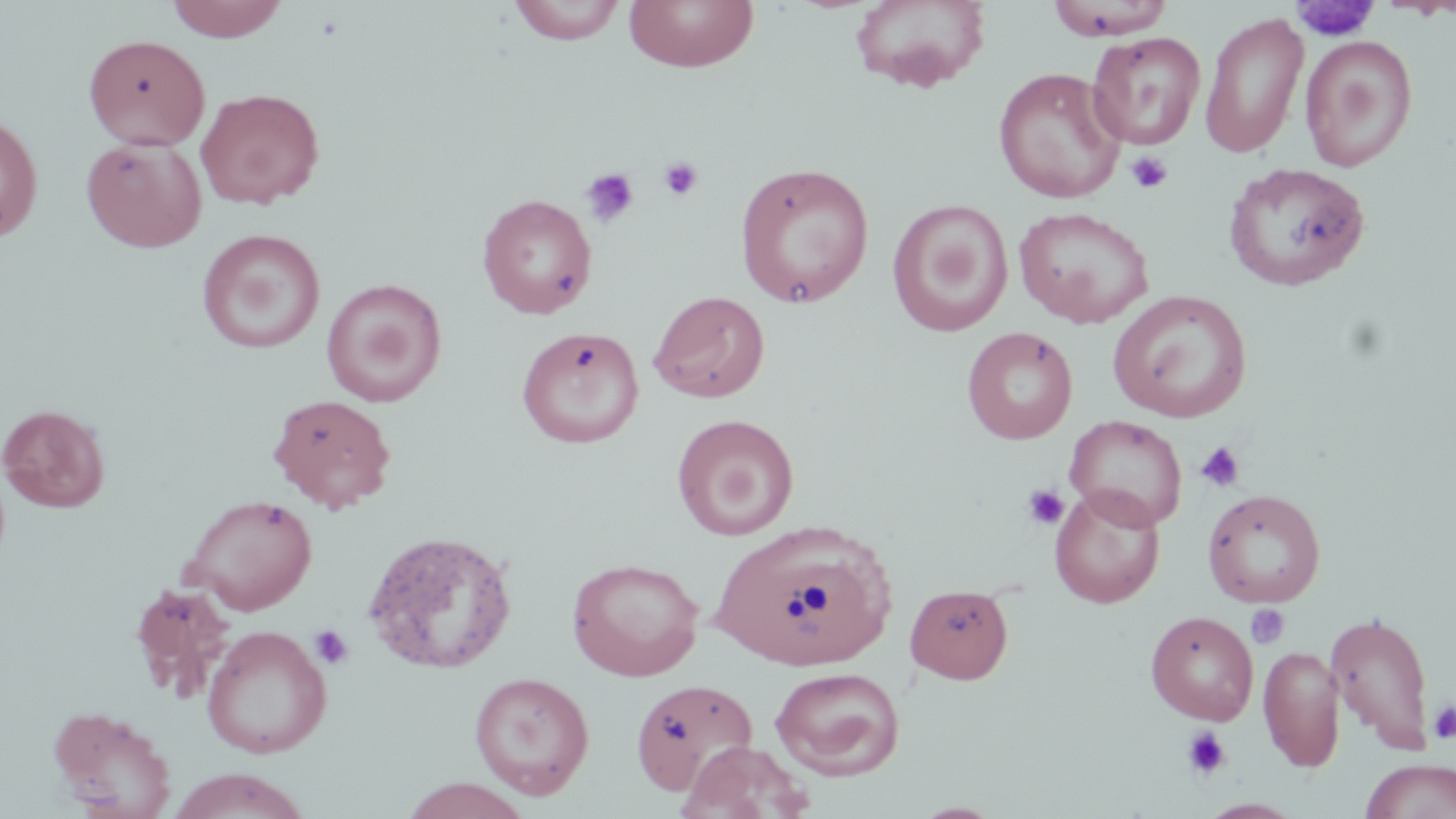

slide_level_diagnosis: negative for blood parasites
modality: light microscopy
magnification: 1000x
preparation: thin blood film
platelet_locations: 'approximate bounding boxes as named x1/y1/x2/y2 corners in pixels: (x1=1291, y1=2, x2=1380, y2=42), (x1=1125, y1=150, x2=1174, y2=194), (x1=657, y1=156, x2=703, y2=201), (x1=580, y1=167, x2=640, y2=228), (x1=1195, y1=440, x2=1246, y2=493), (x1=1021, y1=484, x2=1069, y2=532), (x1=1246, y1=604, x2=1291, y2=649), (x1=309, y1=624, x2=354, y2=670), (x1=1429, y1=701, x2=1456, y2=742), (x1=1180, y1=726, x2=1232, y2=781)'
stain: May-Grünwald-Giemsa
image_size: 1456×819 pixels
uninfected_red_blood_cell_locations: 'approximate bounding boxes as named x1/y1/x2/y2 corners in pixels: (x1=164, y1=0, x2=290, y2=42), (x1=507, y1=0, x2=627, y2=45), (x1=623, y1=0, x2=760, y2=74), (x1=849, y1=0, x2=990, y2=93), (x1=1045, y1=1, x2=1177, y2=39), (x1=1199, y1=10, x2=1310, y2=160), (x1=1087, y1=31, x2=1206, y2=151), (x1=83, y1=34, x2=211, y2=150), (x1=1299, y1=34, x2=1418, y2=172), (x1=992, y1=67, x2=1125, y2=203), (x1=196, y1=87, x2=325, y2=209), (x1=0, y1=111, x2=43, y2=243), (x1=81, y1=135, x2=207, y2=252), (x1=735, y1=161, x2=874, y2=309), (x1=1224, y1=162, x2=1372, y2=292), (x1=477, y1=193, x2=597, y2=319), (x1=886, y1=199, x2=1015, y2=337), (x1=1014, y1=206, x2=1155, y2=328), (x1=197, y1=228, x2=326, y2=354), (x1=321, y1=278, x2=447, y2=406), (x1=649, y1=289, x2=770, y2=403), (x1=1108, y1=289, x2=1252, y2=422), (x1=516, y1=326, x2=644, y2=449), (x1=961, y1=326, x2=1079, y2=445), (x1=268, y1=393, x2=397, y2=513), (x1=0, y1=403, x2=110, y2=513), (x1=671, y1=414, x2=799, y2=541), (x1=1065, y1=415, x2=1187, y2=530), (x1=1049, y1=485, x2=1166, y2=608), (x1=1202, y1=489, x2=1326, y2=608), (x1=180, y1=493, x2=318, y2=615), (x1=713, y1=520, x2=897, y2=672), (x1=362, y1=528, x2=519, y2=675), (x1=567, y1=557, x2=705, y2=681), (x1=905, y1=584, x2=1014, y2=684), (x1=1146, y1=610, x2=1259, y2=726), (x1=1325, y1=610, x2=1436, y2=755), (x1=201, y1=625, x2=332, y2=758), (x1=1258, y1=644, x2=1345, y2=772), (x1=770, y1=666, x2=906, y2=780), (x1=468, y1=672, x2=595, y2=799), (x1=629, y1=678, x2=758, y2=796), (x1=47, y1=704, x2=178, y2=818), (x1=681, y1=740, x2=813, y2=819), (x1=1359, y1=759, x2=1456, y2=819), (x1=166, y1=768, x2=312, y2=819), (x1=400, y1=777, x2=533, y2=818), (x1=1198, y1=798, x2=1303, y2=818), (x1=912, y1=801, x2=1004, y2=818)'
field_of_view: single